State which cell type is depicted.
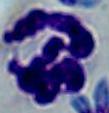

This is a leukocyte.

magnification = 1000x
modality = micrograph